Assess this cell for malaria.
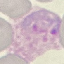
Parasitized.

Summary:
  - Stain: Giemsa
  - Preparation: thin smear
  - Capture: smartphone camera at the microscope eyepiece
  - Image type: cell patch, automatically extracted from a larger field of view and resized to 64 × 64 pixels